Locate every Plasmodium vivax-infected red blood cell.
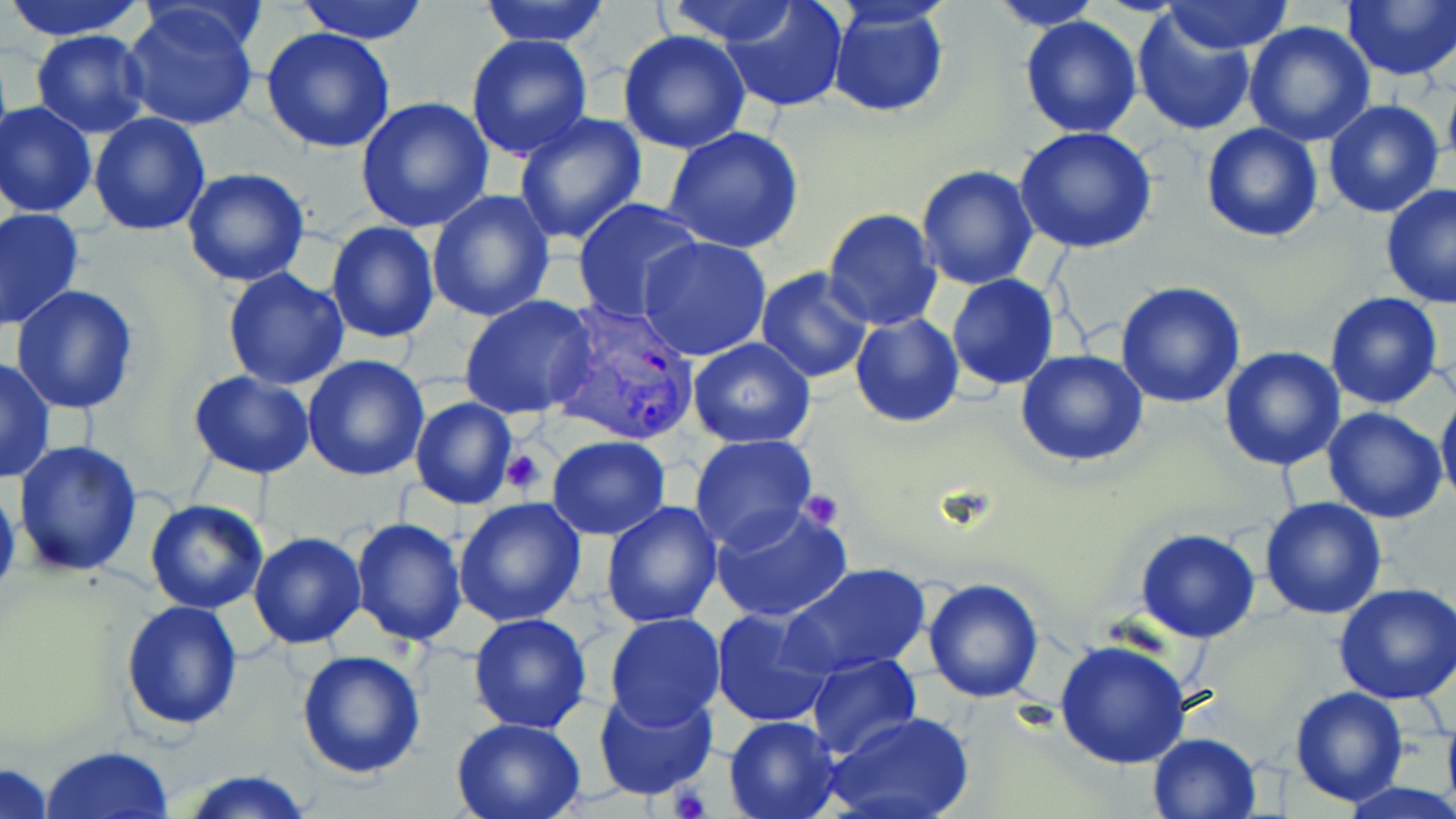
Approximate bounding boxes as (x1, y1, x2, y2) in pixels.
Plasmodium vivax-infected red blood cells: (550, 303, 704, 445).

{
  "slide_level_diagnosis": "Plasmodium vivax",
  "magnification": "1000x",
  "image_size": "1456×819 pixels",
  "field_of_view": "one of a larger specimen",
  "modality": "light microscopy",
  "platelet_locations": "approximate bounding boxes as (x1, y1, x2, y2) in pixels: (499, 446, 549, 498), (798, 490, 844, 530), (668, 786, 711, 819)",
  "uninfected_red_blood_cell_locations": "approximate bounding boxes as (x1, y1, x2, y2) in pixels: (3, 0, 150, 40), (293, 0, 432, 43), (477, 0, 613, 47), (663, 0, 811, 49), (717, 0, 850, 112), (1162, 0, 1295, 54), (1341, 0, 1456, 82), (985, 2, 1107, 31), (827, 5, 950, 117), (120, 6, 262, 132), (1131, 9, 1256, 138), (1020, 15, 1142, 138), (1244, 19, 1375, 144), (261, 27, 397, 153), (29, 29, 151, 137), (617, 31, 752, 154), (466, 34, 595, 161), (1443, 83, 1456, 173), (355, 96, 494, 233), (1323, 100, 1446, 218), (0, 102, 97, 219), (89, 112, 211, 235), (512, 112, 647, 247), (1199, 122, 1324, 242), (662, 125, 805, 254), (1014, 126, 1157, 254), (915, 164, 1039, 289), (182, 168, 310, 288), (1380, 184, 1456, 307), (426, 188, 557, 323), (571, 197, 704, 321), (1, 207, 85, 331), (822, 208, 943, 331), (324, 220, 441, 345), (638, 235, 772, 361), (222, 268, 350, 390), (755, 268, 872, 383), (947, 274, 1060, 390), (1116, 280, 1246, 408), (10, 285, 140, 416), (1324, 292, 1445, 411), (458, 295, 599, 420), (849, 313, 963, 428), (687, 338, 816, 448), (1219, 346, 1347, 470), (1016, 350, 1148, 466), (302, 355, 431, 481), (0, 356, 55, 484), (187, 369, 318, 479), (1437, 386, 1456, 508), (410, 395, 519, 510), (1322, 406, 1447, 523), (688, 433, 817, 551), (548, 436, 671, 540), (14, 440, 143, 576), (0, 477, 21, 610), (453, 497, 586, 627), (1259, 497, 1388, 621), (145, 499, 268, 614), (602, 502, 723, 628), (711, 502, 855, 623), (349, 517, 468, 646), (1133, 529, 1261, 644), (249, 532, 365, 649), (783, 563, 931, 678), (923, 576, 1044, 703), (1333, 581, 1456, 703), (121, 598, 244, 731), (712, 607, 837, 729), (468, 612, 594, 733), (606, 613, 725, 727), (1052, 640, 1194, 769), (295, 649, 426, 779), (804, 653, 922, 759), (592, 684, 719, 802), (1290, 686, 1409, 806), (826, 713, 973, 819), (724, 715, 843, 819), (450, 716, 589, 819), (1148, 732, 1261, 819), (40, 745, 175, 819), (1, 762, 56, 819), (179, 768, 312, 819), (1340, 780, 1456, 819)",
  "stain": "May-Grünwald-Giemsa",
  "preparation": "thin blood film"
}